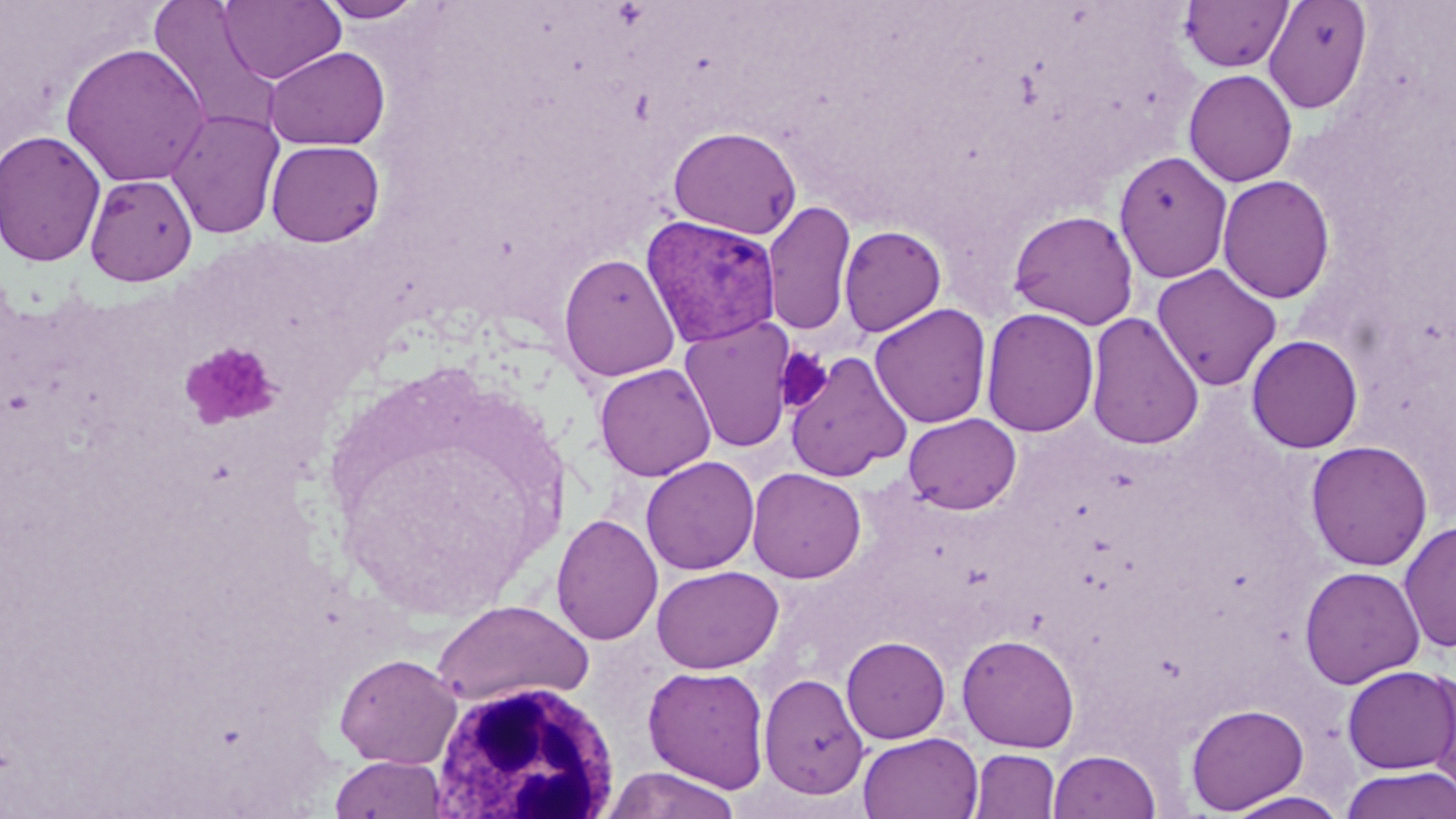

Approximate bounding boxes as (x1, y1, x2, y2) in pixels. White blood cell locations: (428, 678, 622, 818). Uninfected red blood cell locations: (316, 0, 427, 23), (1180, 0, 1293, 72), (1262, 0, 1372, 113), (218, 1, 345, 84), (147, 2, 283, 133), (60, 42, 209, 187), (264, 46, 390, 151), (1183, 69, 1298, 187), (166, 108, 285, 240), (668, 126, 802, 239), (0, 129, 106, 267), (266, 139, 385, 247), (1113, 150, 1233, 284), (85, 173, 197, 286), (1217, 175, 1336, 304), (763, 199, 856, 337), (1007, 209, 1140, 330), (838, 224, 946, 336), (558, 252, 680, 381), (1152, 263, 1283, 391), (869, 303, 992, 429), (980, 306, 1100, 437), (1085, 311, 1204, 450), (679, 317, 796, 454), (1246, 334, 1364, 453), (785, 351, 912, 482), (594, 362, 717, 482), (903, 413, 1021, 514), (1305, 440, 1433, 571), (640, 456, 760, 575), (747, 467, 867, 583), (551, 513, 663, 646), (1399, 519, 1456, 654), (651, 565, 783, 673), (1299, 565, 1425, 689), (430, 599, 594, 709), (957, 633, 1080, 753), (841, 636, 950, 743), (334, 653, 462, 768), (643, 665, 770, 793), (1342, 665, 1456, 774), (1424, 668, 1456, 800), (758, 673, 869, 799), (1186, 703, 1309, 814), (858, 732, 983, 818), (968, 749, 1060, 818), (1048, 749, 1161, 819), (329, 755, 450, 817), (602, 766, 743, 819), (1341, 766, 1456, 819), (1224, 791, 1349, 818). Plasmodium vivax-infected red blood cell locations: (641, 215, 781, 348). Platelet locations: (180, 341, 281, 430), (774, 347, 832, 412). Slide-level diagnosis: Plasmodium vivax. Captured at 1000x magnification. Light microscopy. Thin blood smear. Single field of view. Image is 1456×819 pixels. May-Grünwald-Giemsa-stained preparation.